Report the malaria status of this cell.
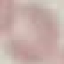

It is uninfected.

Summary:
  - Stain: Giemsa
  - Image type: automatically extracted cell patch, resized to 64 × 64 pixels
  - Capture: smartphone through the microscope eyepiece
  - Preparation: thin blood smear